Describe the morphology of the red blood cells.
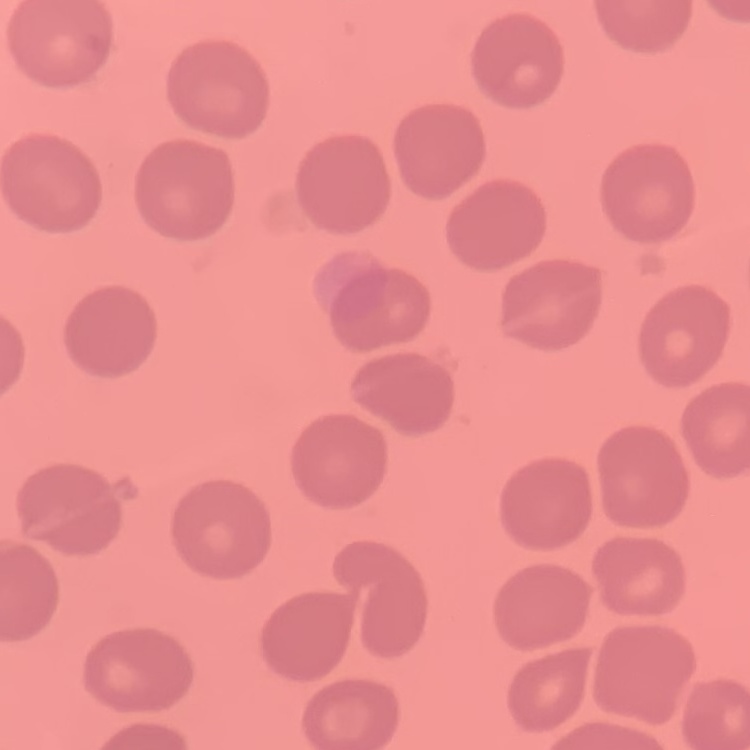
They show no rouleaux formation.

Summary:
  - Stain: Field's or Giemsa
  - Preparation: thin blood film
  - Image type: square crop of a larger photomicrograph